Classify this cell by malaria status.
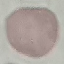
It is uninfected.

Summary:
  - Image type: automatically extracted cell patch, resized to 64 × 64 pixels
  - Preparation: thin smear
  - Capture: smartphone through the microscope eyepiece
  - Stain: Giemsa